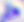
Toxoplasma gondii is shown. 400x magnification. Micrograph.